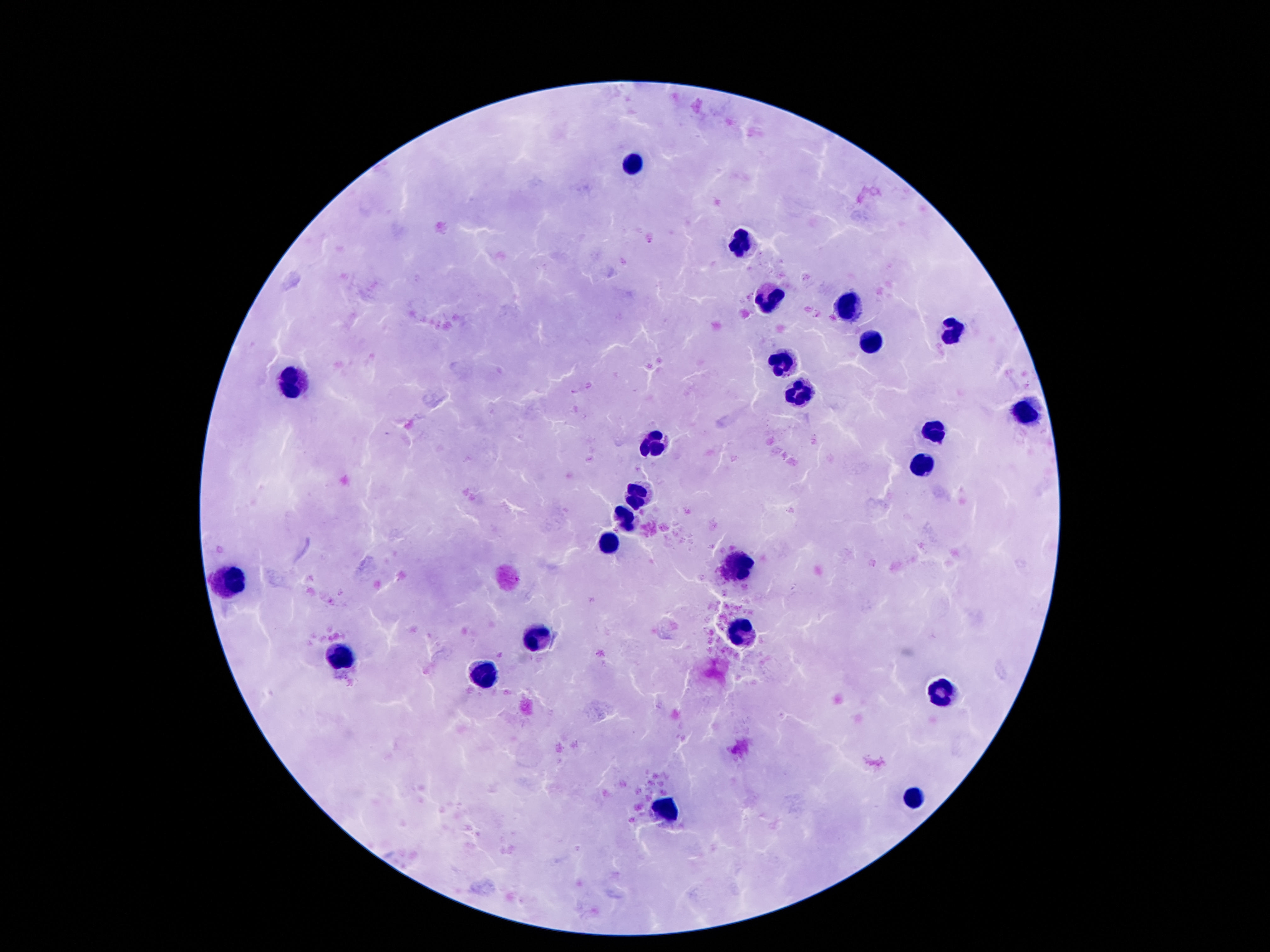
Approximate object centers, in pixels from the top-left corner.
Summary:
  - Leukocyte locations: (x=633, y=164), (x=743, y=246), (x=770, y=298), (x=852, y=307), (x=952, y=333), (x=871, y=341), (x=782, y=364), (x=291, y=380), (x=799, y=395), (x=1026, y=410), (x=934, y=429), (x=654, y=442), (x=921, y=465), (x=638, y=494), (x=627, y=519), (x=608, y=543), (x=734, y=568), (x=230, y=582), (x=740, y=630), (x=537, y=636), (x=341, y=655), (x=486, y=674), (x=946, y=691), (x=911, y=800), (x=665, y=808)
  - Preparation: thick blood smear
  - Image size: 1270×952 pixels
  - Capture: smartphone camera through the microscope eyepiece
  - Stain: Giemsa
  - Magnification: 100x
  - Patient malaria status: not infected
  - Field of view: single